Assess this cell for malaria.
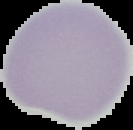

Uninfected.

Summary:
  - Image size: 133×130 pixels
  - Preparation: thin blood film
  - Image type: segmented cell region on a black background